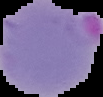
From a thin blood film. Malaria status: parasitized. Image is 103×97 pixels. Segmented cell region on a black background.